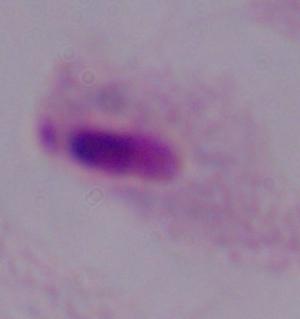

magnification = 1000x
identification = trichomonad
modality = micrograph